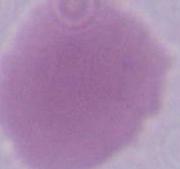
Summary:
  - Modality: photomicrograph
  - Identification: red blood cell
  - Magnification: 1000x